Report the malaria status of this cell.
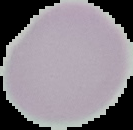
Uninfected.

Image is 133×130 pixels. Segmented cell region on a black background. From a thin blood smear.